Report the malaria status of this cell.
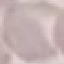
It is uninfected.

preparation = thin blood smear
image type = automatically extracted cell patch, resized to 64 × 64 pixels
stain = Giemsa
capture = smartphone through the microscope eyepiece